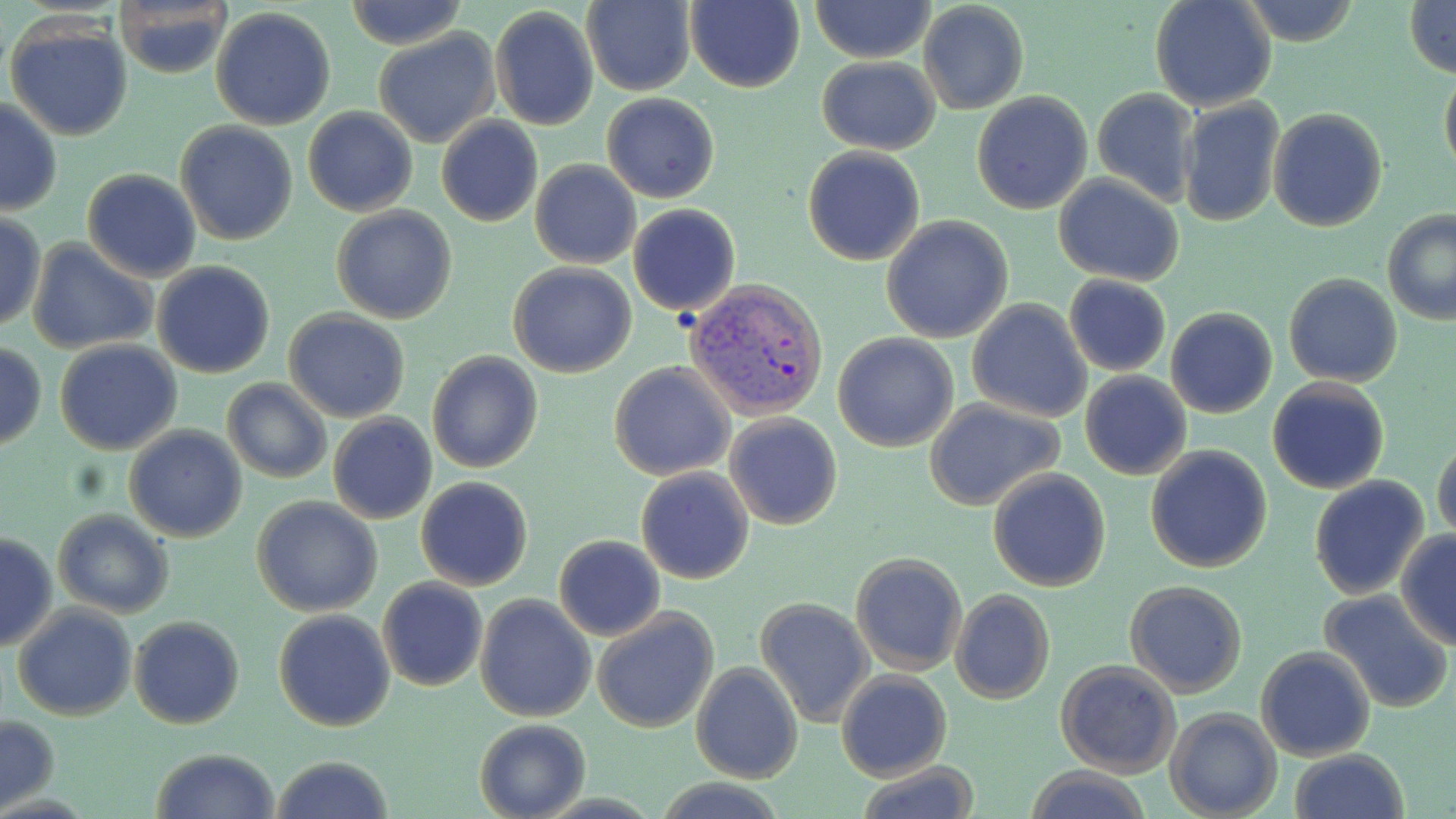
slide_level_diagnosis: Plasmodium vivax
preparation: thin blood film
field_of_view: one of a larger specimen
uninfected_red_blood_cell_locations: 'approximate bounding boxes as (x1,y1)-(x2,y2) corner pairs in pixels: (344,0)-(467,51), (684,0)-(805,91), (811,0)-(935,63), (1405,0)-(1456,76), (580,1)-(695,94), (1150,1)-(1277,112), (110,2)-(232,79), (918,2)-(1027,114), (1236,2)-(1364,47), (489,5)-(598,131), (211,7)-(338,130), (6,17)-(134,143), (373,30)-(500,148), (817,56)-(940,154), (1439,60)-(1456,180), (1092,87)-(1200,207), (971,91)-(1093,213), (602,92)-(720,203), (0,97)-(63,216), (1179,99)-(1284,227), (302,107)-(418,216), (1268,108)-(1387,232), (436,116)-(543,228), (175,121)-(300,245), (803,147)-(925,265), (531,160)-(641,269), (82,168)-(200,281), (1052,173)-(1183,286), (627,203)-(740,317), (332,206)-(457,325), (1383,210)-(1456,325), (0,211)-(45,333), (880,216)-(1014,343), (26,240)-(156,355), (151,261)-(276,380), (508,263)-(637,379), (1283,273)-(1402,388), (1064,274)-(1170,376), (966,299)-(1092,422), (1165,307)-(1279,418), (284,309)-(412,422), (832,333)-(958,453), (54,340)-(183,454), (0,341)-(47,451), (426,351)-(543,475), (610,362)-(736,480), (1079,371)-(1192,480), (221,378)-(331,484), (1267,379)-(1392,495), (925,399)-(1064,511), (724,412)-(843,529), (327,414)-(438,524), (125,426)-(248,543), (1432,433)-(1456,545), (1145,445)-(1273,573), (635,468)-(755,584), (988,469)-(1111,591), (1307,475)-(1430,599), (415,476)-(534,591), (252,497)-(383,618), (53,510)-(174,618), (1,529)-(57,654), (1395,529)-(1456,650), (553,535)-(666,641), (850,552)-(967,676), (377,578)-(487,692), (1125,581)-(1249,697), (949,589)-(1055,705), (1318,589)-(1452,713), (475,594)-(596,722), (755,597)-(874,726), (11,602)-(137,721), (591,608)-(718,733), (273,609)-(395,731), (129,616)-(245,729), (1256,647)-(1376,762), (1054,660)-(1181,777), (690,663)-(803,783), (836,670)-(953,781), (1165,708)-(1283,819), (1,713)-(58,814), (475,717)-(591,819), (149,749)-(279,819), (1289,749)-(1410,819), (271,755)-(395,819), (853,762)-(983,818), (1022,767)-(1152,819), (652,779)-(788,819)'
image_size: 1456×819 pixels
plasmodium_vivax_infected_red_blood_cell_locations: 'approximate bounding boxes as (x1,y1)-(x2,y2) corner pairs in pixels: (682,278)-(827,419)'
stain: May-Grünwald-Giemsa
modality: optical microscopy
magnification: 1000x